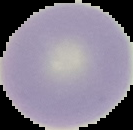
image type = segmented cell region with the area outside set to black
result = no Plasmodium parasites seen
preparation = thin blood film
image size = 133×130 pixels